State which parasite is depicted.
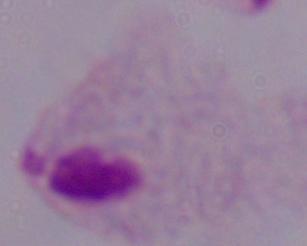

This is a trichomonad.

magnification = 1000x
modality = photomicrograph